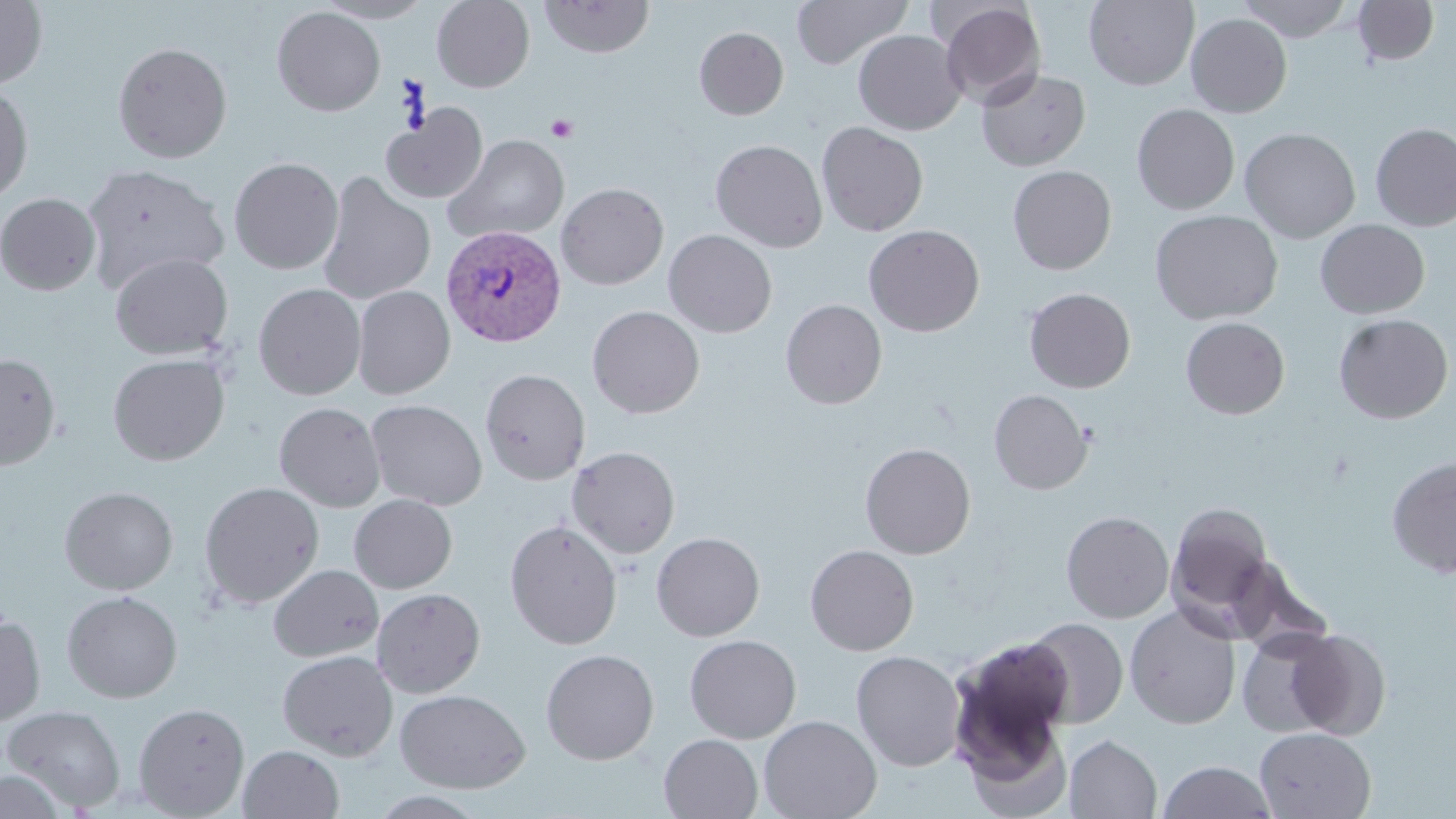

slide_level_diagnosis: Plasmodium vivax
magnification: 1000x
image_size: 1456×819 pixels
stain: May-Grünwald-Giemsa
preparation: thin blood smear
field_of_view: single
platelet_locations: 'approximate bounding boxes as named x1/y1/x2/y2 corners in pixels: (x1=546, y1=115, x2=578, y2=142)'
plasmodium_vivax_infected_red_blood_cell_locations: 'approximate bounding boxes as named x1/y1/x2/y2 corners in pixels: (x1=441, y1=225, x2=565, y2=347)'
modality: optical microscopy
uninfected_red_blood_cell_locations: 'approximate bounding boxes as named x1/y1/x2/y2 corners in pixels: (x1=313, y1=0, x2=433, y2=23), (x1=432, y1=0, x2=535, y2=92), (x1=539, y1=0, x2=655, y2=58), (x1=792, y1=0, x2=913, y2=69), (x1=1084, y1=0, x2=1199, y2=90), (x1=1237, y1=0, x2=1355, y2=42), (x1=1353, y1=0, x2=1440, y2=66), (x1=0, y1=1, x2=48, y2=88), (x1=936, y1=1, x2=1046, y2=109), (x1=272, y1=6, x2=386, y2=117), (x1=1186, y1=13, x2=1292, y2=118), (x1=694, y1=27, x2=788, y2=119), (x1=853, y1=30, x2=966, y2=134), (x1=112, y1=41, x2=232, y2=163), (x1=976, y1=67, x2=1090, y2=171), (x1=0, y1=80, x2=34, y2=204), (x1=1132, y1=103, x2=1240, y2=214), (x1=382, y1=105, x2=487, y2=203), (x1=817, y1=122, x2=928, y2=236), (x1=1371, y1=122, x2=1456, y2=231), (x1=1239, y1=127, x2=1360, y2=243), (x1=443, y1=134, x2=570, y2=244), (x1=710, y1=139, x2=828, y2=252), (x1=229, y1=157, x2=343, y2=275), (x1=82, y1=162, x2=229, y2=291), (x1=1007, y1=165, x2=1116, y2=274), (x1=317, y1=172, x2=436, y2=305), (x1=556, y1=182, x2=668, y2=289), (x1=0, y1=193, x2=101, y2=295), (x1=1149, y1=209, x2=1284, y2=325), (x1=1315, y1=219, x2=1429, y2=319), (x1=864, y1=224, x2=985, y2=336), (x1=664, y1=229, x2=777, y2=338), (x1=109, y1=252, x2=233, y2=359), (x1=253, y1=283, x2=366, y2=400), (x1=353, y1=285, x2=455, y2=399), (x1=1024, y1=287, x2=1136, y2=392), (x1=781, y1=299, x2=887, y2=409), (x1=587, y1=306, x2=704, y2=418), (x1=1333, y1=313, x2=1454, y2=424), (x1=1180, y1=317, x2=1289, y2=419), (x1=0, y1=353, x2=61, y2=470), (x1=108, y1=353, x2=229, y2=466), (x1=480, y1=369, x2=590, y2=485), (x1=989, y1=389, x2=1092, y2=494), (x1=366, y1=399, x2=487, y2=510), (x1=274, y1=402, x2=385, y2=512), (x1=860, y1=442, x2=975, y2=559), (x1=567, y1=446, x2=680, y2=558), (x1=1387, y1=455, x2=1456, y2=578), (x1=199, y1=482, x2=324, y2=608), (x1=59, y1=486, x2=178, y2=595), (x1=349, y1=494, x2=457, y2=593), (x1=358, y1=494, x2=467, y2=698), (x1=1167, y1=502, x2=1276, y2=629), (x1=1061, y1=510, x2=1174, y2=623), (x1=504, y1=519, x2=623, y2=650), (x1=651, y1=532, x2=765, y2=641), (x1=804, y1=544, x2=919, y2=656), (x1=267, y1=564, x2=383, y2=662), (x1=372, y1=587, x2=485, y2=698), (x1=62, y1=590, x2=183, y2=702), (x1=1125, y1=603, x2=1241, y2=729), (x1=0, y1=614, x2=45, y2=727), (x1=1022, y1=617, x2=1129, y2=729), (x1=1236, y1=629, x2=1343, y2=738), (x1=1282, y1=629, x2=1391, y2=739), (x1=684, y1=634, x2=802, y2=743), (x1=949, y1=635, x2=1076, y2=766), (x1=540, y1=649, x2=659, y2=764), (x1=277, y1=650, x2=398, y2=761), (x1=850, y1=650, x2=966, y2=771), (x1=395, y1=688, x2=530, y2=793), (x1=133, y1=702, x2=250, y2=817), (x1=2, y1=705, x2=126, y2=811), (x1=955, y1=706, x2=1073, y2=819), (x1=758, y1=715, x2=882, y2=819), (x1=1255, y1=727, x2=1376, y2=818), (x1=658, y1=734, x2=763, y2=819), (x1=1064, y1=735, x2=1162, y2=818), (x1=239, y1=745, x2=345, y2=819), (x1=1157, y1=760, x2=1277, y2=819), (x1=0, y1=769, x2=68, y2=819)'